Give the position of every leukocyte visible.
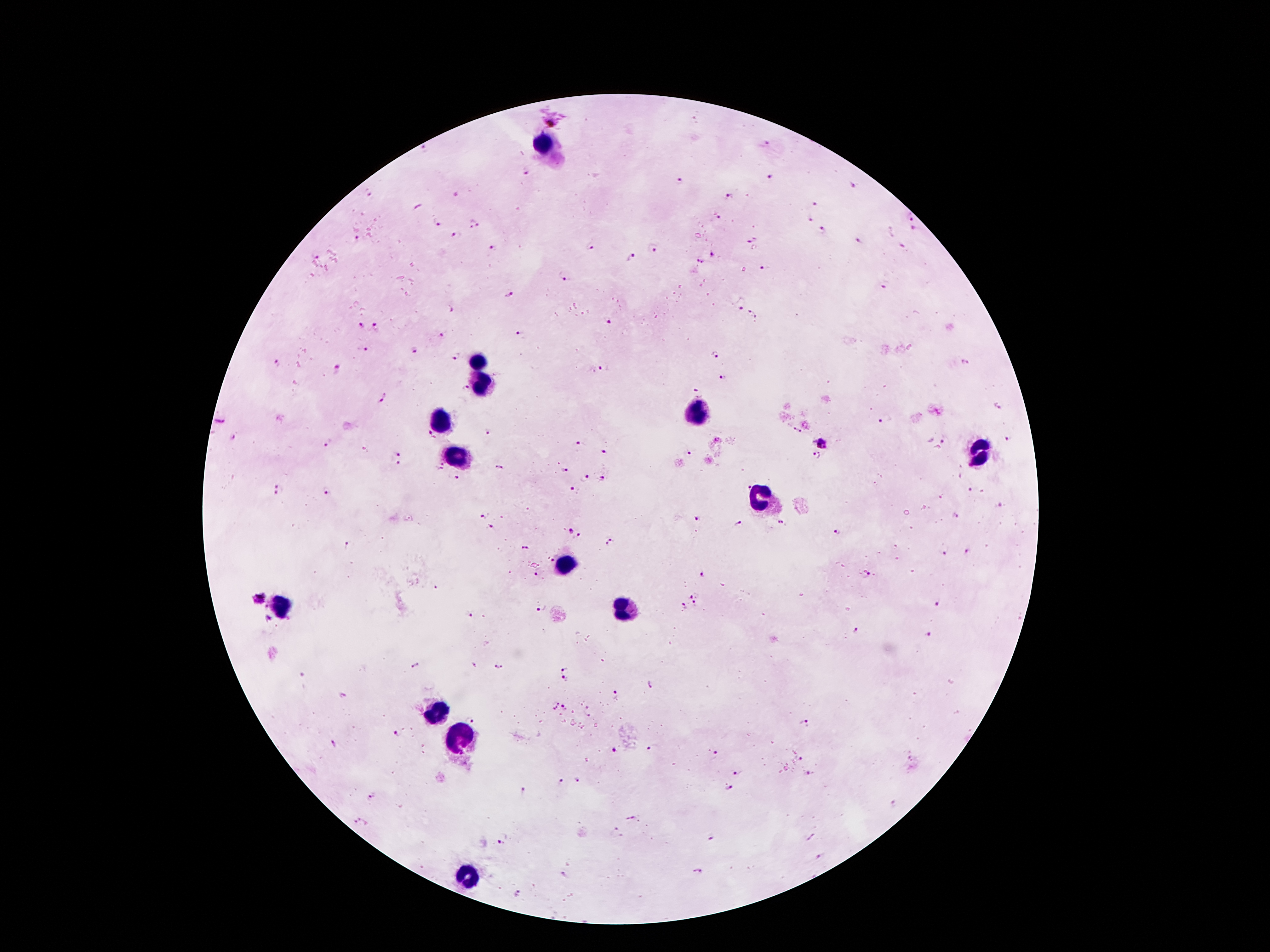

Approximate object centers, in pixels from the top-left corner.
Leukocytes: (x=545, y=144), (x=476, y=359), (x=484, y=384), (x=694, y=413), (x=440, y=419), (x=980, y=450), (x=455, y=458), (x=761, y=497), (x=566, y=564), (x=281, y=605), (x=623, y=611), (x=436, y=713), (x=466, y=741), (x=464, y=876).

Malaria parasite locations: (x=552, y=115), (x=766, y=144), (x=425, y=150), (x=526, y=173), (x=773, y=178), (x=682, y=182), (x=853, y=185), (x=368, y=193), (x=728, y=198), (x=814, y=204), (x=718, y=216), (x=910, y=217), (x=810, y=220), (x=436, y=223), (x=473, y=225), (x=822, y=230), (x=914, y=230), (x=455, y=236), (x=357, y=239), (x=858, y=239), (x=752, y=240), (x=591, y=245), (x=902, y=245), (x=654, y=247), (x=492, y=248), (x=716, y=254), (x=317, y=257), (x=631, y=257), (x=701, y=260), (x=762, y=267), (x=564, y=276), (x=887, y=284), (x=509, y=293), (x=740, y=309), (x=452, y=310), (x=752, y=314), (x=608, y=322), (x=361, y=325), (x=376, y=326), (x=443, y=335), (x=519, y=335), (x=363, y=348), (x=414, y=350), (x=715, y=356), (x=454, y=358), (x=965, y=361), (x=277, y=363), (x=338, y=368), (x=603, y=368), (x=724, y=378), (x=463, y=388), (x=699, y=390), (x=382, y=398), (x=999, y=406), (x=885, y=419), (x=220, y=420), (x=796, y=431), (x=486, y=433), (x=430, y=435), (x=233, y=438), (x=1008, y=439), (x=944, y=440), (x=579, y=442), (x=821, y=443), (x=326, y=445), (x=605, y=449), (x=399, y=454), (x=688, y=455), (x=817, y=457), (x=397, y=465), (x=498, y=466), (x=441, y=467), (x=565, y=472), (x=456, y=477), (x=584, y=477), (x=601, y=479), (x=746, y=485), (x=279, y=490), (x=969, y=490), (x=574, y=491), (x=328, y=494), (x=482, y=515), (x=956, y=516), (x=696, y=517), (x=781, y=522), (x=738, y=523), (x=490, y=526), (x=838, y=530), (x=570, y=531), (x=578, y=534), (x=612, y=542), (x=348, y=545), (x=524, y=547), (x=944, y=551), (x=967, y=551), (x=553, y=559), (x=536, y=574), (x=702, y=574), (x=866, y=574), (x=435, y=588), (x=258, y=597), (x=691, y=597), (x=940, y=603), (x=695, y=604), (x=265, y=605), (x=683, y=607), (x=540, y=609), (x=469, y=617), (x=267, y=619), (x=856, y=630), (x=927, y=634), (x=415, y=664), (x=499, y=665), (x=566, y=666), (x=300, y=675), (x=564, y=679), (x=651, y=683), (x=616, y=694), (x=344, y=697), (x=554, y=707), (x=565, y=708), (x=588, y=710), (x=470, y=719), (x=803, y=723), (x=397, y=733), (x=334, y=743), (x=650, y=748), (x=612, y=750), (x=713, y=750), (x=801, y=758), (x=739, y=771), (x=809, y=774), (x=579, y=781), (x=562, y=782), (x=729, y=789), (x=523, y=792), (x=371, y=796), (x=893, y=803), (x=631, y=817), (x=358, y=820), (x=616, y=833), (x=710, y=838), (x=501, y=845), (x=698, y=871), (x=564, y=874), (x=519, y=893). Photographed through the microscope eyepiece with a smartphone camera. Image is 1270×952 pixels. Single field of view. Thick peripheral-blood smear. 100x magnification. Patient malaria status: positive for Plasmodium falciparum. Giemsa-stained preparation.